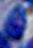
magnification = 1000x
modality = micrograph
identification = Toxoplasma gondii